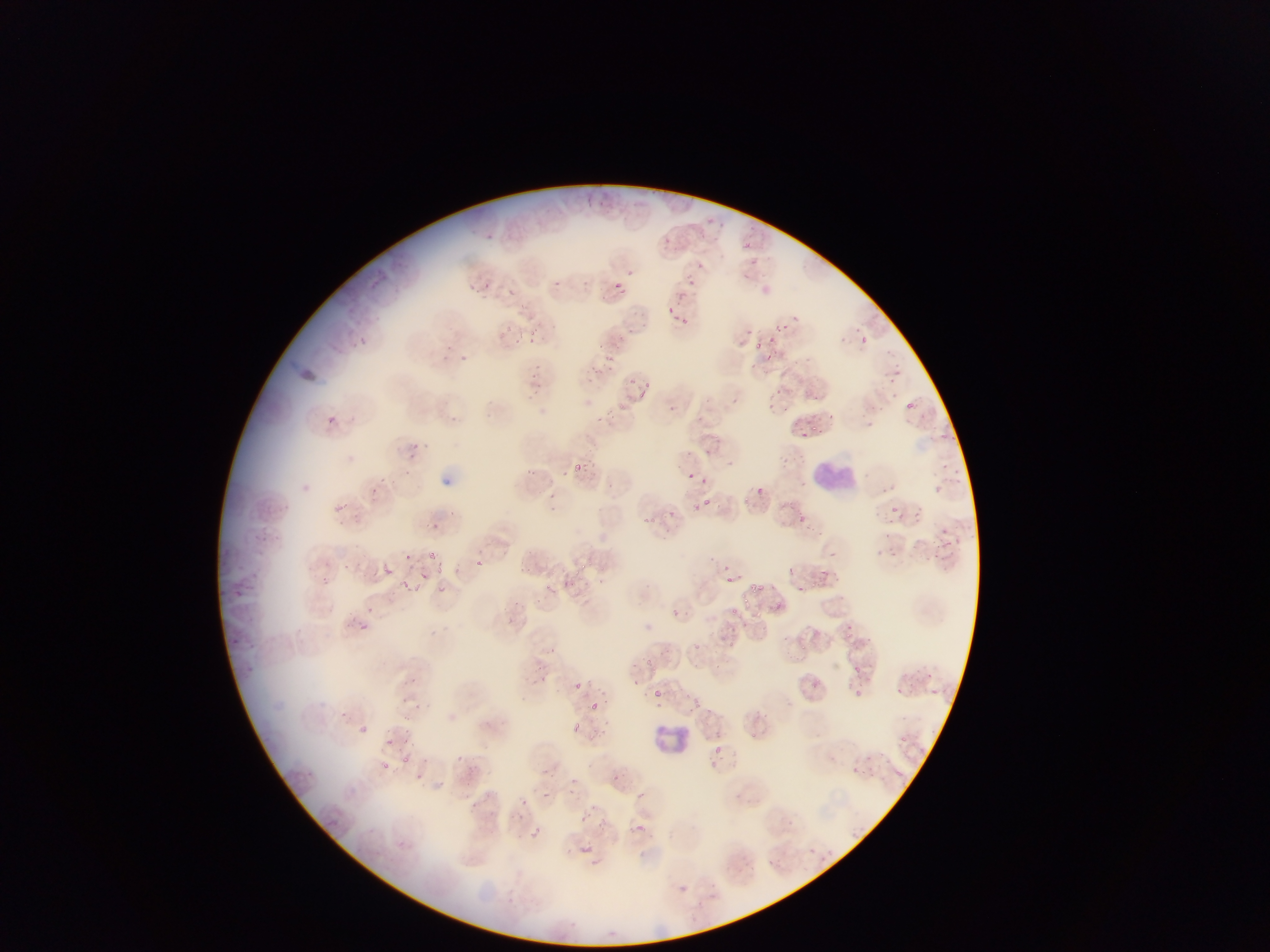 Approximate bounding boxes as (left, top, right, bottom) in pixels. Leukocyte locations: (811, 457, 854, 498), (659, 720, 710, 764). Plasmodium parasite locations: (486, 233, 495, 242), (665, 237, 669, 246), (741, 238, 754, 256), (687, 279, 697, 289), (554, 280, 560, 288), (613, 282, 626, 295), (506, 287, 517, 296), (677, 291, 689, 302), (675, 315, 687, 325), (781, 322, 791, 332), (614, 332, 627, 345), (769, 332, 780, 344), (864, 337, 872, 344), (528, 338, 535, 347), (753, 340, 766, 352), (443, 342, 454, 351), (603, 354, 613, 364), (591, 367, 600, 374), (529, 372, 543, 383), (643, 381, 653, 389), (639, 390, 646, 400), (905, 401, 915, 410), (618, 402, 624, 410), (326, 415, 339, 426), (811, 422, 817, 432), (802, 430, 810, 440), (940, 431, 957, 446), (410, 443, 420, 451), (584, 458, 598, 468), (573, 463, 583, 473), (524, 465, 536, 476), (945, 470, 957, 484), (687, 471, 694, 480), (755, 482, 764, 496), (936, 485, 944, 496), (742, 495, 752, 504), (700, 499, 712, 509), (331, 503, 350, 513), (890, 505, 900, 514), (797, 513, 805, 523), (644, 516, 654, 525), (939, 527, 956, 547), (429, 553, 439, 561), (403, 554, 416, 565), (577, 558, 591, 574), (475, 560, 484, 568), (435, 562, 446, 573), (382, 566, 392, 576), (819, 567, 838, 583), (419, 571, 427, 584), (727, 575, 736, 582), (401, 579, 417, 593), (544, 581, 554, 595), (752, 581, 766, 593), (437, 584, 446, 593), (794, 585, 807, 595), (742, 596, 752, 606), (776, 602, 783, 612), (366, 605, 375, 614), (730, 607, 742, 618), (839, 628, 869, 656), (730, 638, 744, 650), (689, 642, 706, 658), (801, 642, 809, 656), (547, 646, 556, 654), (643, 655, 655, 667), (854, 666, 862, 675), (575, 682, 584, 689), (654, 690, 662, 697), (855, 690, 861, 700), (694, 698, 706, 708), (591, 700, 601, 710), (599, 719, 609, 735), (572, 724, 581, 732), (360, 725, 368, 733), (898, 734, 909, 743), (402, 754, 414, 765), (380, 761, 393, 776), (895, 769, 903, 776), (570, 779, 578, 786), (540, 789, 550, 799), (636, 791, 645, 799), (521, 799, 529, 808), (581, 815, 590, 825), (328, 817, 338, 827), (635, 823, 645, 832), (533, 826, 540, 837), (396, 840, 407, 851), (580, 845, 594, 850), (591, 859, 603, 864) | approximate (x, y) pixel centers of objects too small to bound: (700, 265), (630, 271), (671, 308), (381, 480), (704, 481), (814, 683), (718, 748). Thin blood smear. Image is 1270×952 pixels. Single field of view. Mobile-phone photograph taken through the microscope. Collected in Ghana.